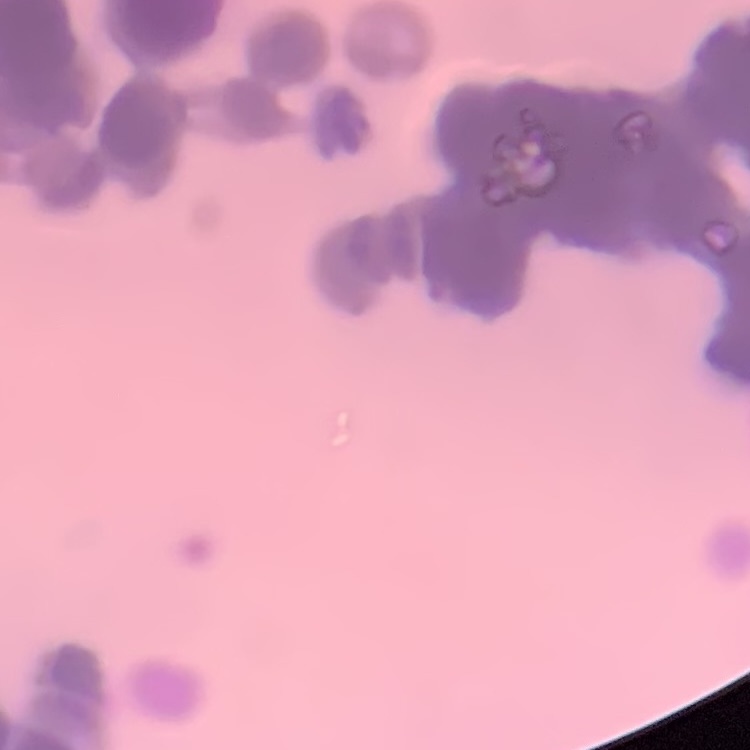
The erythrocytes show rouleaux formation. Stained with either Field's or Giemsa. Thin blood smear. One tile cut from a larger photomicrograph.